Mark where leukocytes are.
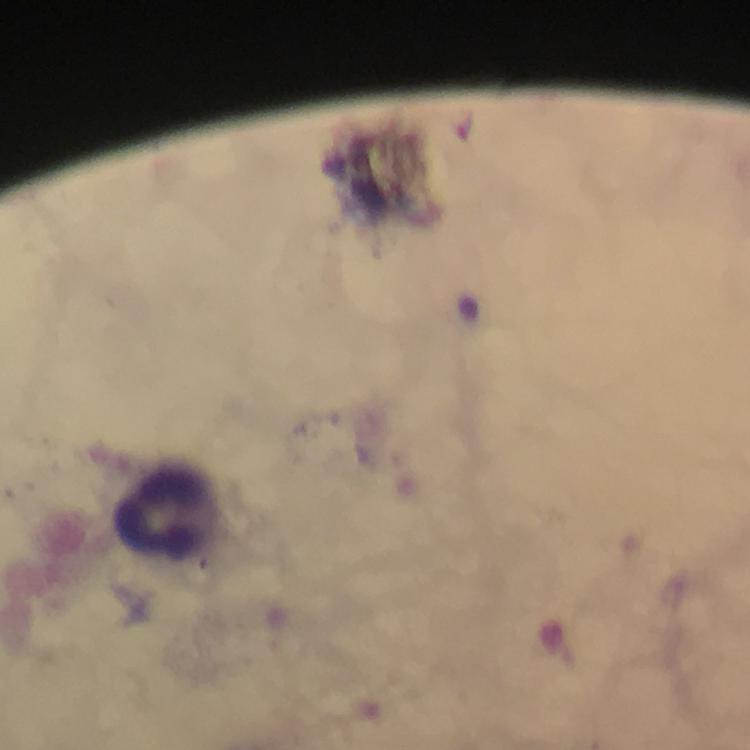

Approximate centers as {x, y} in pixels.
Leukocytes: {171, 514}.

Image is 750×750 pixels. Photographed through the microscope with a smartphone camera. Immersion oil applied. Thick blood smear. Giemsa stain. At 100x magnification. From a diagnostic examination for malaria. Cropped region of a single field of view. Plasmodium parasites: none detected.